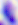
Summary:
  - Identification: Toxoplasma gondii
  - Magnification: 400x
  - Modality: micrograph